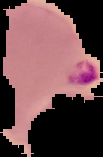
From a thin blood film. Image is 103×157 pixels. Malaria status: parasitized. The area outside the segmented cell region is set to black.